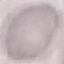 Result: no malaria parasites detected. Giemsa-stained preparation. Acquired by smartphone through the microscope eyepiece. Cell patch, automatically extracted from a larger field of view and resized to 64 × 64 pixels. Thin smear of blood.